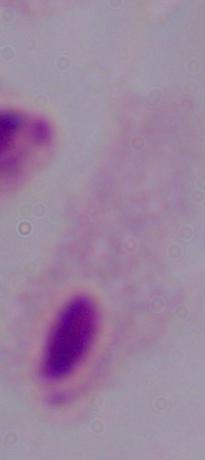
modality = micrograph
magnification = 1000x
identification = trichomonad